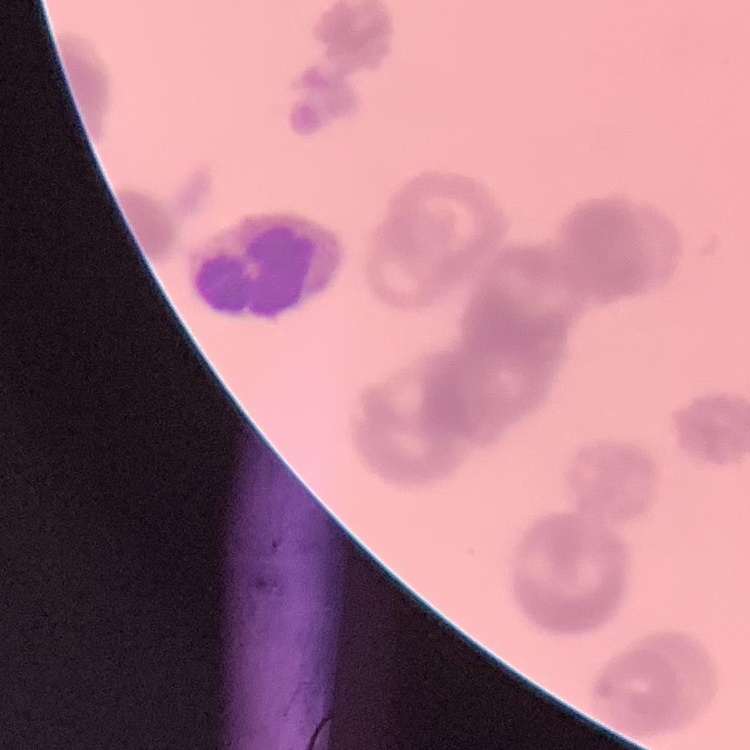

erythrocyte morphology = rouleaux formation
image type = one tile cut from a larger photomicrograph
stain = Field's or Giemsa
preparation = thin blood smear